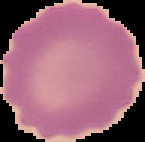
image size = 145×142 pixels
malaria status = uninfected
preparation = thin blood smear
image type = segmented cell region on a black background